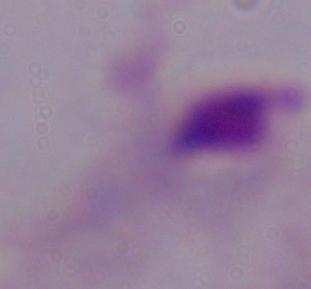

Summary:
  - Modality: photomicrograph
  - Identification: trichomonad
  - Magnification: 1000x